Report the malaria status of this cell.
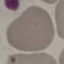
Uninfected.

Summary:
  - Capture: smartphone through the microscope eyepiece
  - Preparation: thin smear
  - Image type: cell patch, automatically extracted from a larger field of view and resized to 64 × 64 pixels
  - Stain: Giemsa